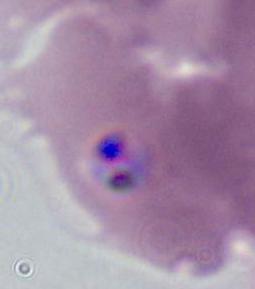
magnification: 400x or 1000x
modality: photomicrograph
identification: Plasmodium